Identify the parasite.
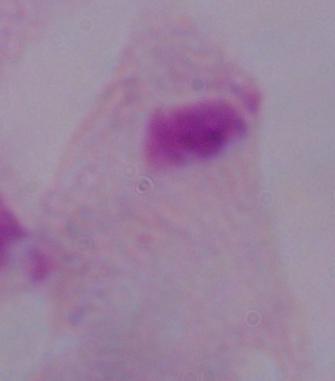
A trichomonad.

{
  "magnification": "1000x",
  "modality": "micrograph"
}